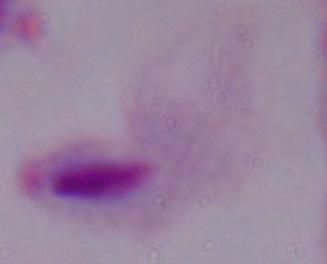

Summary:
  - Identification: trichomonad
  - Magnification: 1000x
  - Modality: micrograph